Evaluate for malaria.
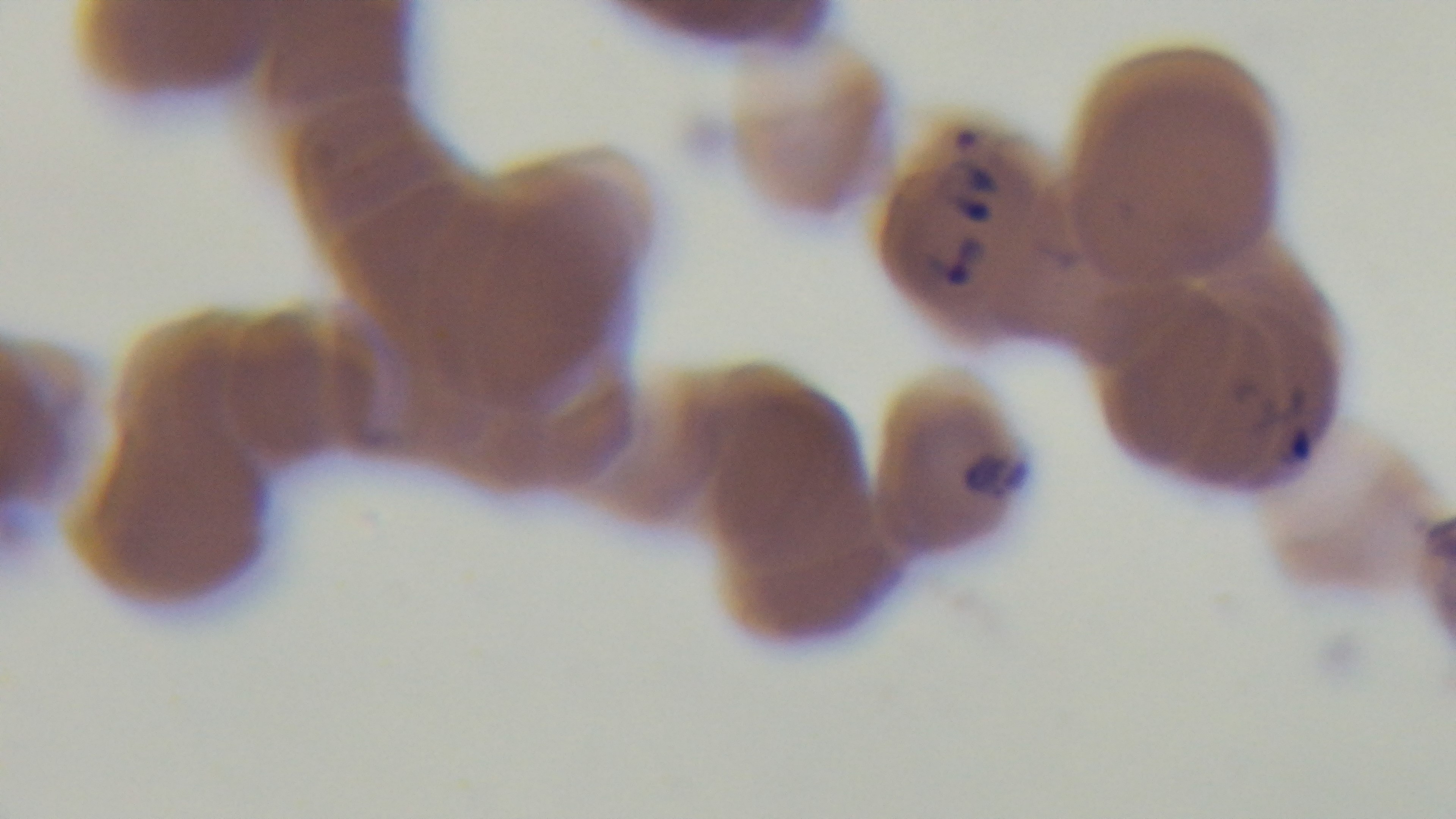
It is infected.

{
  "stain": "Giemsa",
  "preparation": "thin",
  "objective": "100x oil immersion",
  "modality": "light microscopy",
  "field_of_view": "one from the slide",
  "capture": "mounted 4K digital camera"
}